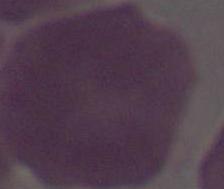
1000x magnification. An erythrocyte is seen. Photomicrograph.